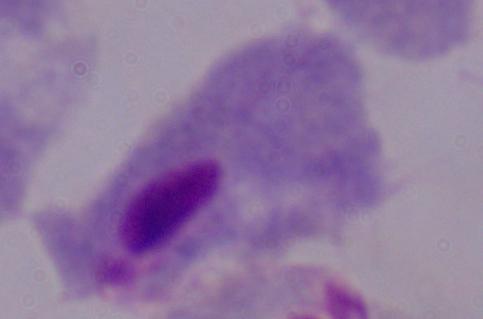

magnification = 1000x
modality = micrograph
identification = trichomonad